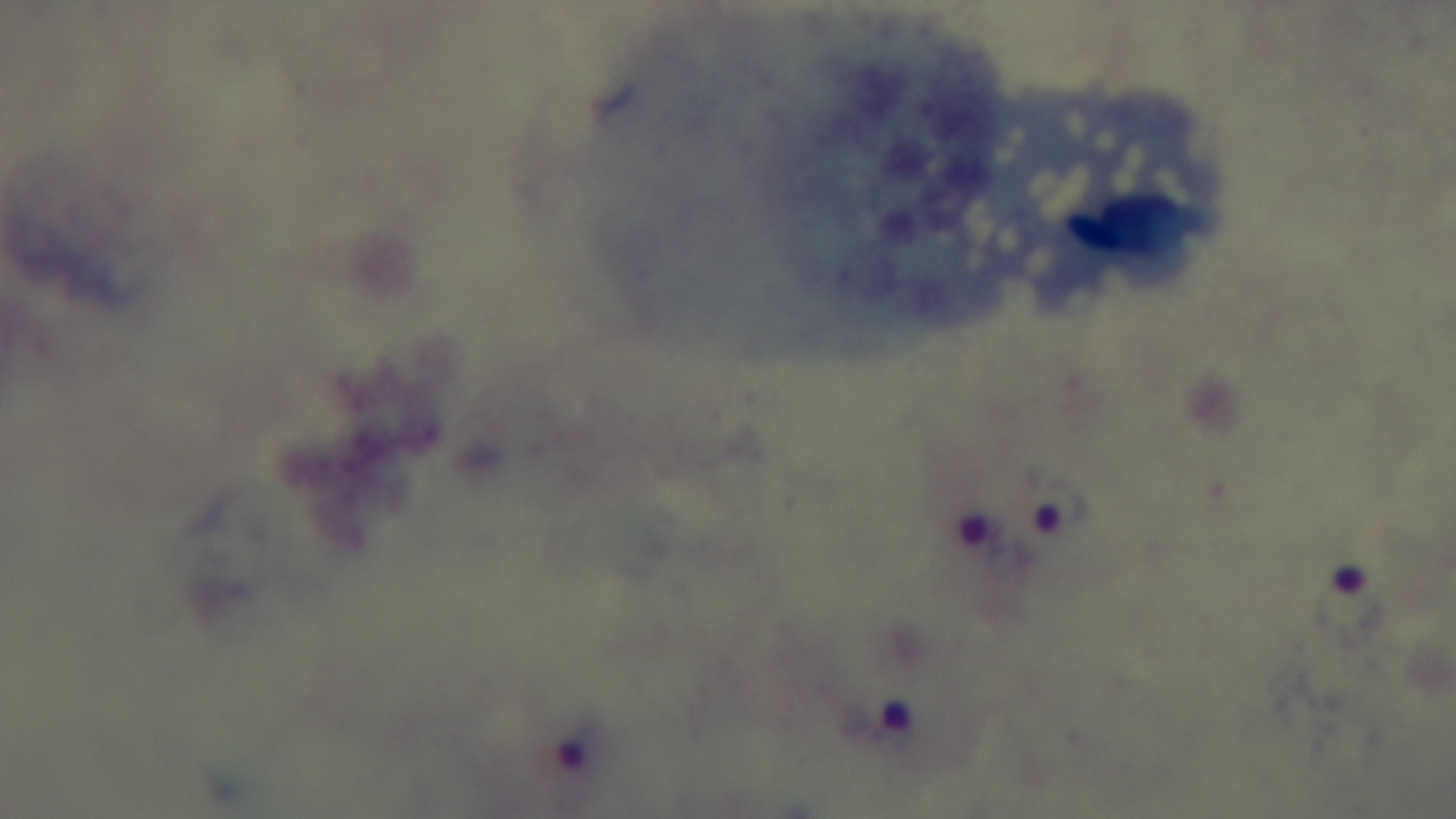
Summary:
  - Stain: Giemsa
  - Field of view: one from the slide
  - Objective: 100x oil immersion
  - Modality: light microscopy
  - Capture: mounted 4K digital camera
  - Malaria status: positive
  - Preparation: thick